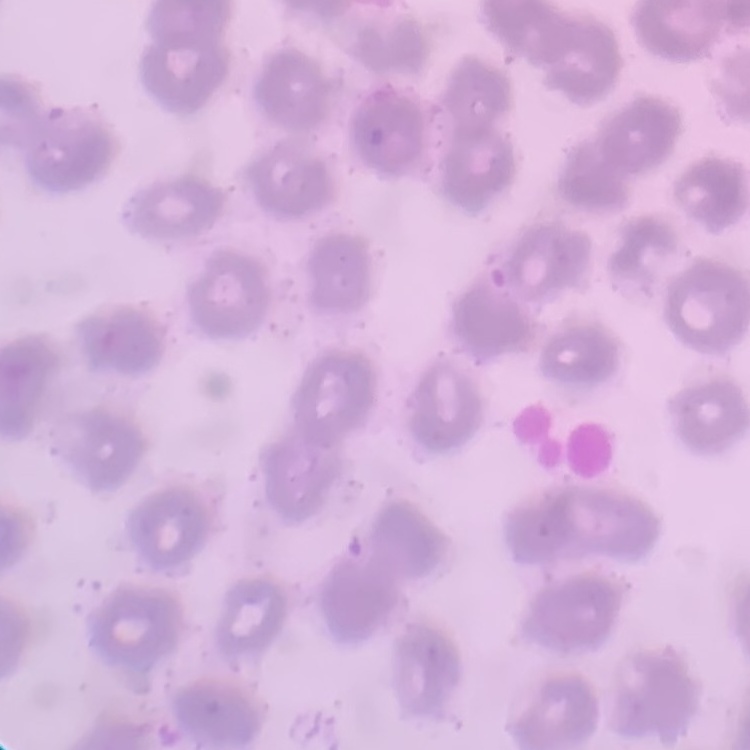

Summary:
  - Erythrocyte morphology: no rouleaux formation
  - Image type: one tile cut from a larger photomicrograph
  - Stain: Field's or Giemsa
  - Preparation: thin blood smear